Locate and identify every blood parasite.
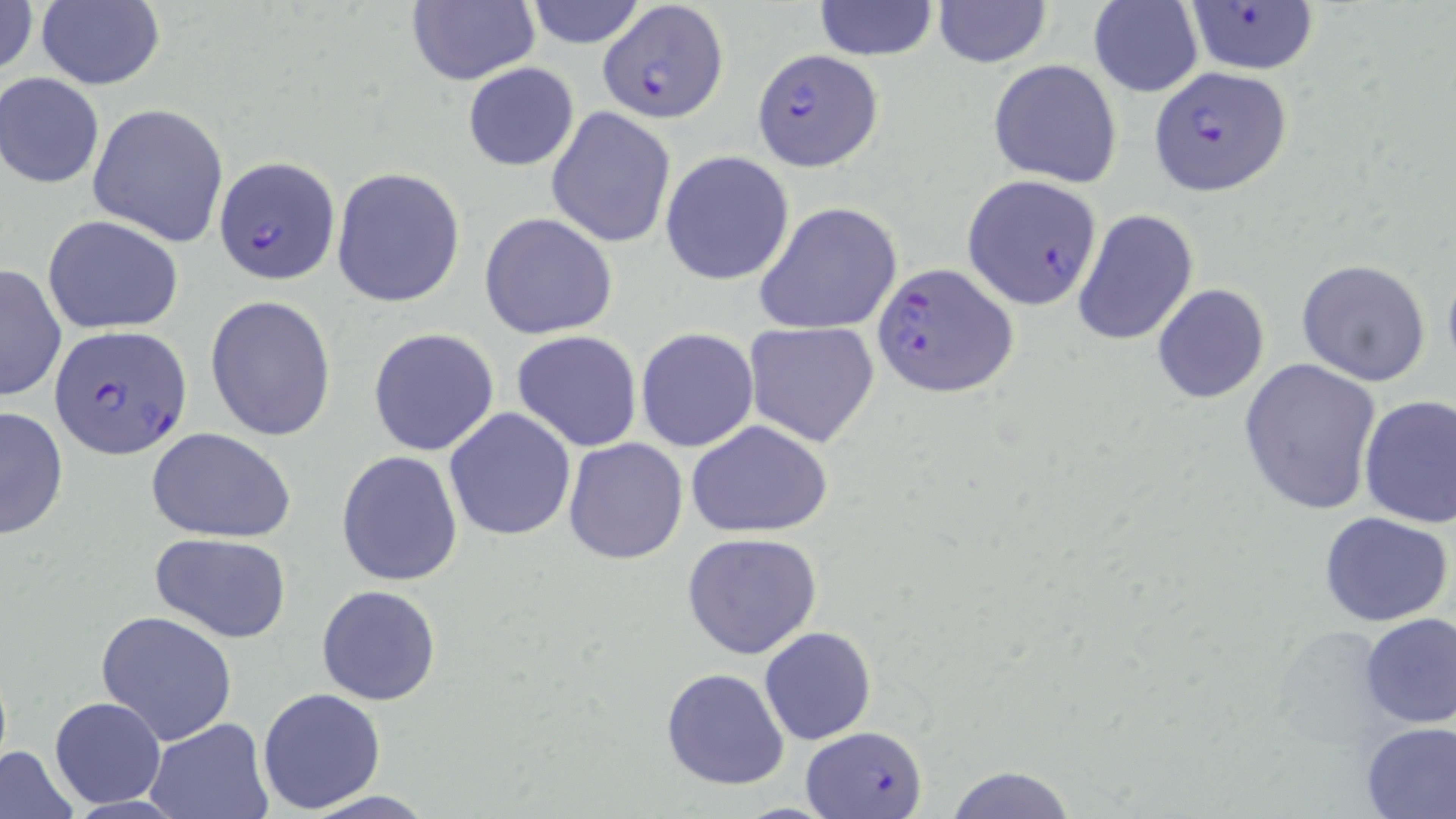

Approximate bounding boxes as (x1, y1, x2, y2) in pixels.
Plasmodium falciparum-infected red blood cells: (597, 0, 727, 124), (1184, 3, 1317, 75), (752, 49, 882, 169), (1148, 66, 1293, 196), (213, 156, 342, 286), (961, 174, 1103, 308), (872, 261, 1018, 399), (49, 325, 192, 460), (800, 726, 928, 817).
No Plasmodium ovale, Plasmodium malariae, Plasmodium vivax, Babesia divergens, or Trypanosoma brucei observed.

slide-level diagnosis = Plasmodium falciparum
magnification = 1000x
uninfected red blood cell locations = approximate bounding boxes as (x1, y1, x2, y2) in pixels: (0, 0, 40, 83), (36, 0, 165, 89), (523, 0, 646, 48), (403, 1, 540, 88), (932, 1, 1053, 68), (812, 2, 939, 59), (1086, 2, 1203, 97), (988, 59, 1125, 188), (462, 63, 579, 171), (1, 73, 104, 188), (86, 102, 229, 248), (545, 107, 677, 250), (660, 151, 796, 287), (331, 167, 466, 307), (754, 202, 903, 336), (1071, 208, 1200, 346), (479, 213, 620, 339), (43, 215, 186, 334), (1441, 255, 1456, 384), (1296, 259, 1432, 387), (0, 263, 68, 401), (1152, 283, 1270, 404), (204, 295, 336, 441), (742, 321, 881, 448), (635, 327, 759, 451), (367, 328, 500, 457), (511, 331, 643, 451), (1240, 358, 1383, 517), (1358, 395, 1456, 529), (0, 405, 69, 540), (444, 407, 577, 542), (684, 419, 834, 537), (146, 425, 297, 543), (564, 437, 689, 565), (336, 450, 463, 587), (1319, 512, 1453, 627), (681, 532, 823, 660), (150, 533, 293, 643), (317, 585, 442, 706), (95, 610, 238, 746), (1357, 611, 1456, 729), (759, 627, 879, 746), (660, 667, 790, 791), (257, 688, 387, 813), (48, 696, 168, 809), (145, 718, 272, 818), (1359, 721, 1455, 818), (0, 745, 82, 819), (941, 765, 1078, 819), (297, 790, 443, 819)
field of view = one of a larger specimen
image size = 1456×819 pixels
stain = May-Grünwald-Giemsa
modality = optical microscopy
preparation = thin blood smear